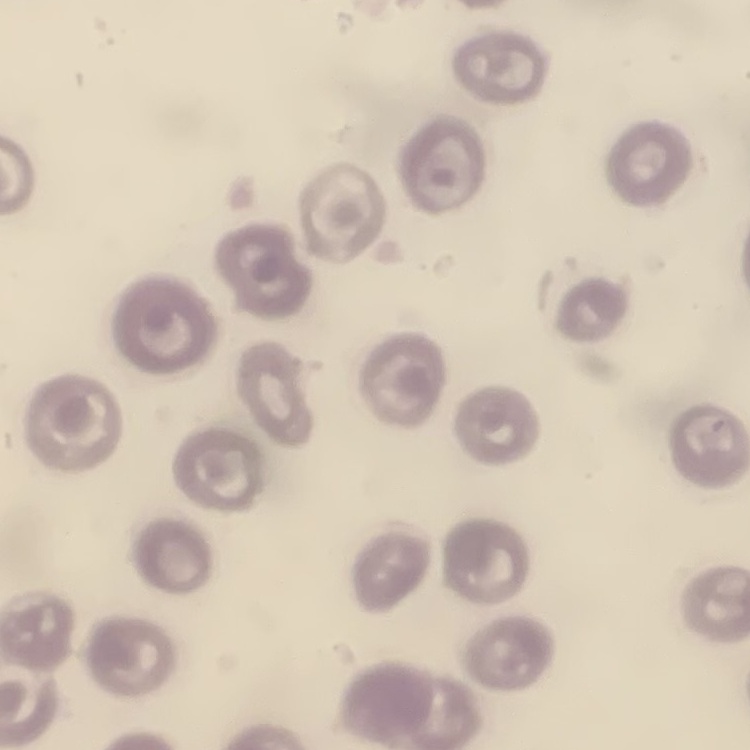
Summary:
  - Red blood cell morphology: no rouleaux formation
  - Stain: Field's or Giemsa
  - Image type: one tile cut from a larger photomicrograph
  - Preparation: thin blood smear